Assess this cell for malaria.
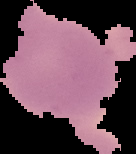

It is uninfected.

Summary:
  - Image size: 136×154 pixels
  - Image type: segmented cell region on a black background
  - Preparation: thin blood film